Classify this cell by malaria status.
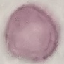

It is uninfected.

image type = automatically extracted cell patch, resized to 64 × 64 pixels
stain = Giemsa
capture = smartphone camera at the microscope eyepiece
preparation = thin smear